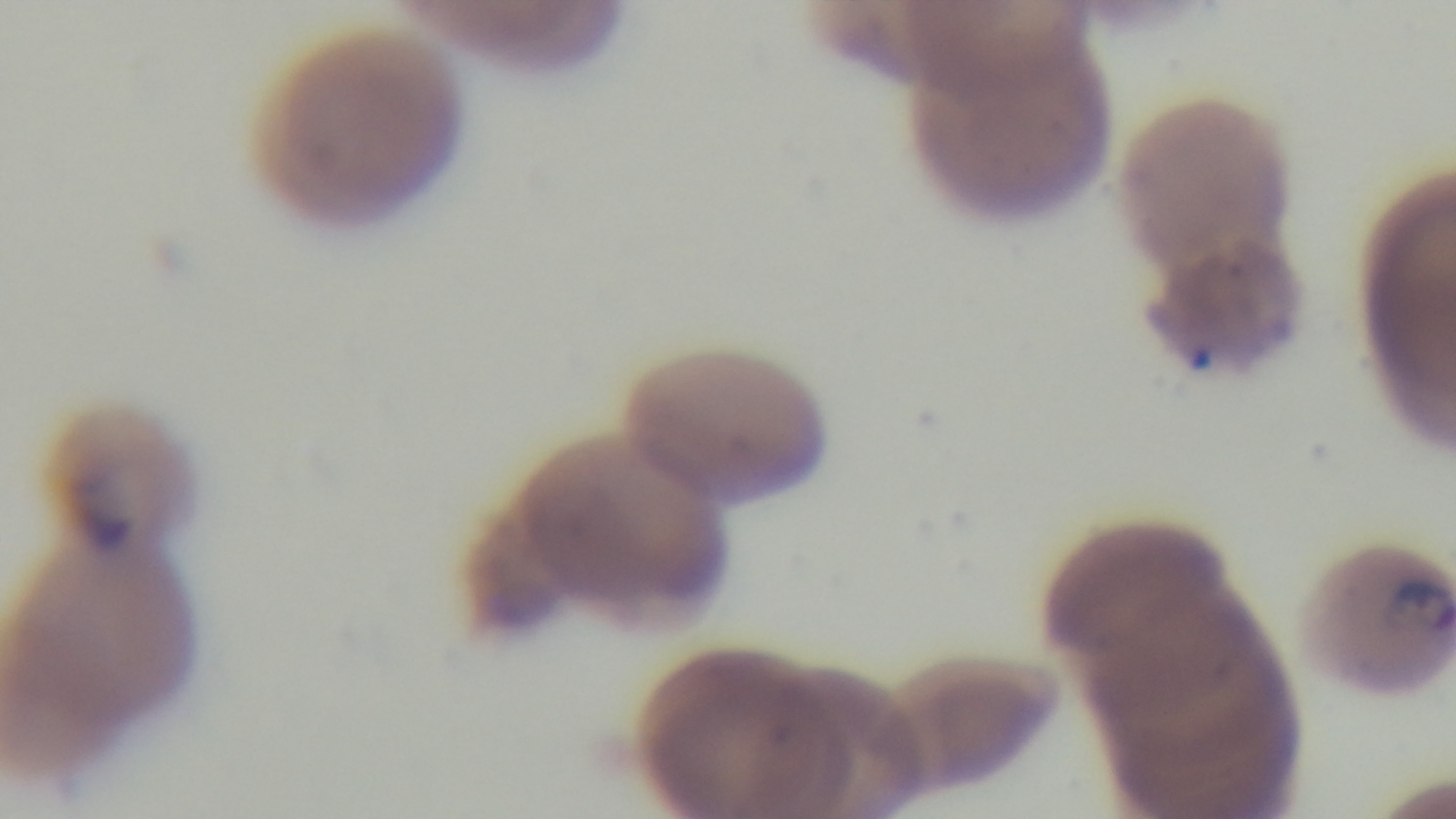
objective = 100x oil immersion
field of view = one from the slide
capture = mounted 4K digital camera
preparation = thin
stain = Giemsa
modality = light microscopy
malaria status = infected